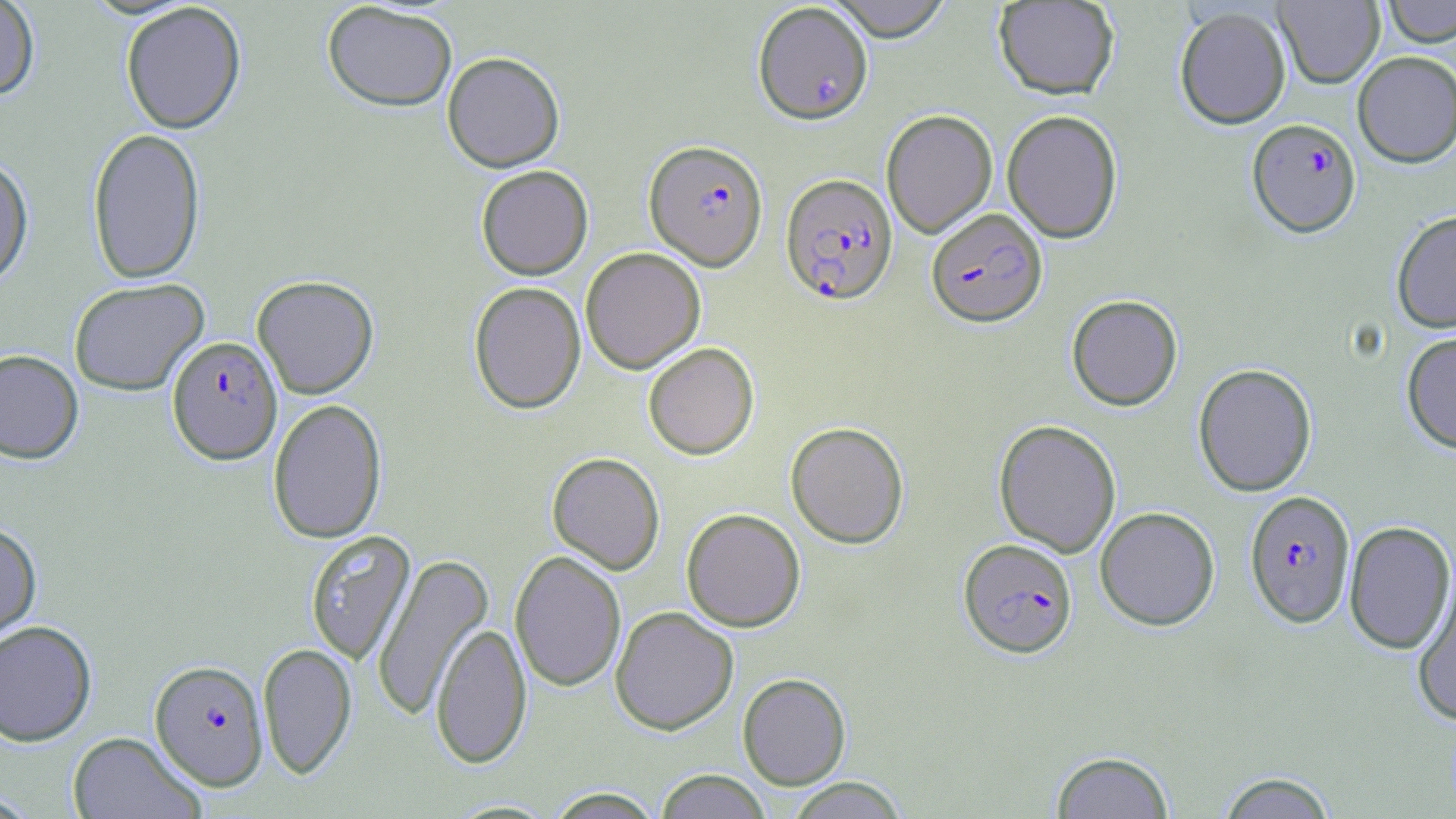
Summary:
  - Coordinate format: approximate bounding boxes as [x1, y1, x2, y2] in pixels
  - Uninfected red blood cell locations: [0, 0, 40, 101], [825, 0, 954, 41], [1274, 0, 1384, 88], [1382, 0, 1456, 47], [993, 1, 1119, 99], [321, 2, 457, 112], [120, 3, 247, 134], [1174, 6, 1291, 129], [442, 51, 565, 171], [1353, 51, 1456, 168], [881, 109, 998, 238], [1002, 109, 1123, 243], [87, 127, 206, 285], [0, 154, 34, 287], [476, 164, 593, 279], [1392, 210, 1456, 333], [580, 247, 706, 374], [252, 275, 379, 399], [69, 277, 209, 395], [468, 281, 586, 414], [1066, 294, 1183, 411], [1401, 331, 1456, 454], [643, 342, 759, 459], [0, 349, 83, 463], [1193, 363, 1317, 497], [268, 398, 388, 543], [993, 419, 1121, 557], [785, 421, 909, 548], [547, 452, 665, 574], [1095, 507, 1220, 631], [681, 508, 805, 632], [1343, 521, 1455, 655], [0, 522, 42, 642], [305, 530, 416, 666], [510, 550, 626, 692], [372, 552, 494, 721], [1412, 567, 1456, 726], [610, 606, 738, 734], [0, 620, 97, 746], [431, 622, 532, 769], [257, 642, 356, 778], [738, 673, 851, 789], [68, 731, 205, 819], [1050, 750, 1175, 818], [653, 769, 772, 818], [1216, 771, 1339, 818], [784, 777, 910, 818], [545, 788, 663, 818]
  - Plasmodium falciparum-infected red blood cell locations: [752, 3, 873, 124], [1247, 118, 1361, 238], [644, 139, 767, 271], [780, 173, 897, 305], [926, 208, 1047, 327], [168, 335, 282, 464], [1244, 490, 1356, 628], [958, 538, 1078, 658], [150, 659, 269, 790]
  - Slide-level diagnosis: Plasmodium falciparum
  - Magnification: 1000x
  - Stain: May-Grünwald-Giemsa
  - Field of view: single
  - Modality: optical microscopy
  - Preparation: thin blood film
  - Image size: 1456×819 pixels